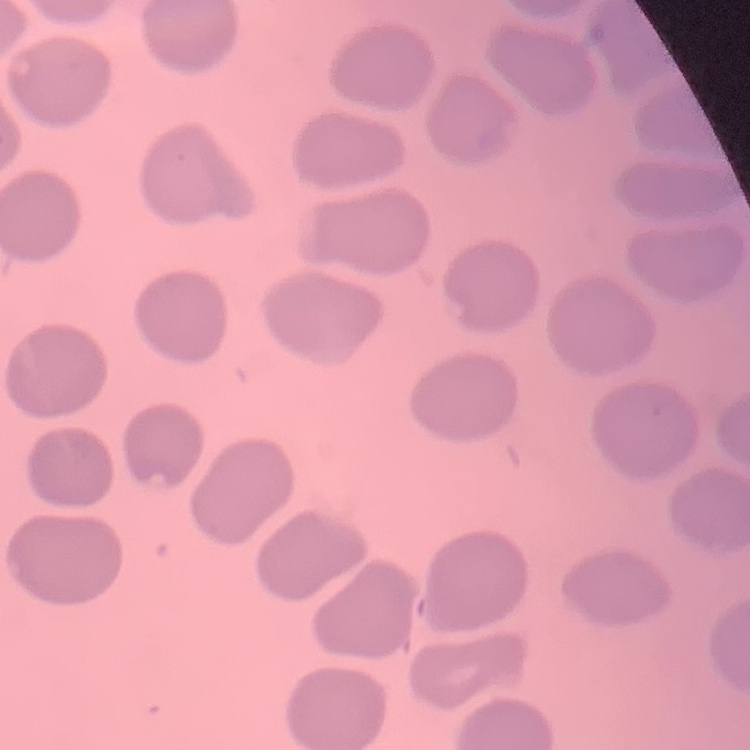

red blood cell morphology = no rouleaux formation
preparation = thin peripheral smear
stain = Field's or Giemsa
image type = square crop of a larger photomicrograph